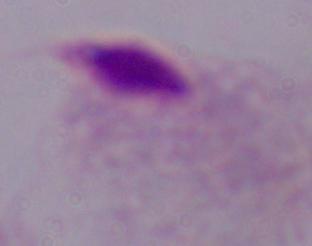
Summary:
  - Magnification: 1000x
  - Identification: trichomonad
  - Modality: micrograph